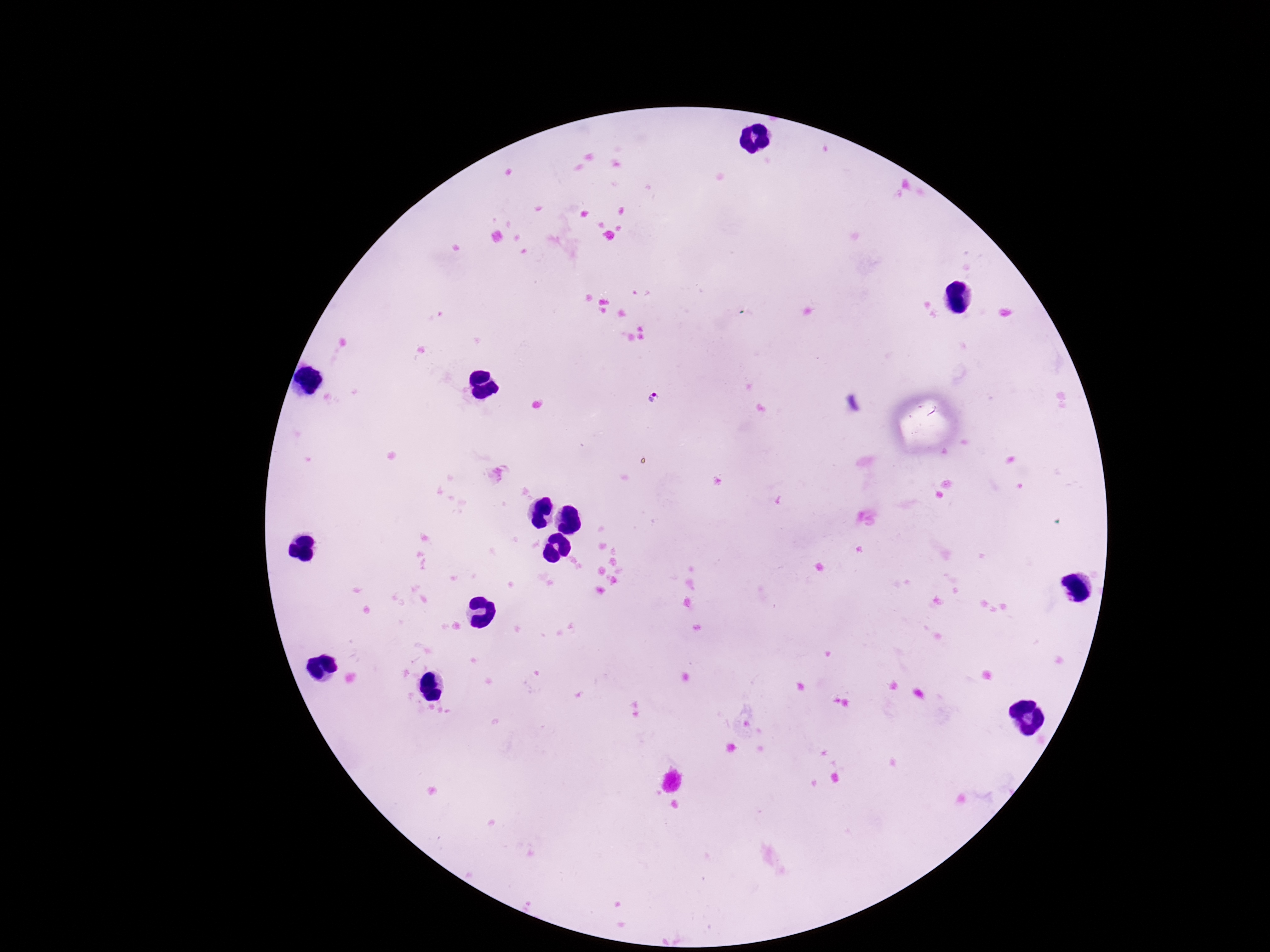 Approximate object centers, in pixels from the top-left corner. Plasmodium parasite locations: (x=654, y=395). Giemsa stain. Thick peripheral-blood smear. Image is 1270×952 pixels. Patient malaria status: positive. Smartphone photograph taken through the microscope eyepiece. 100x magnification. One field from this slide.